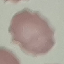
{
  "malaria_status": "uninfected",
  "preparation": "thin blood film",
  "capture": "smartphone camera at the microscope eyepiece",
  "image_type": "cell patch, automatically extracted from a larger field of view and resized to 64 × 64 pixels",
  "stain": "Giemsa"
}